Locate every blood parasite and identify its species.
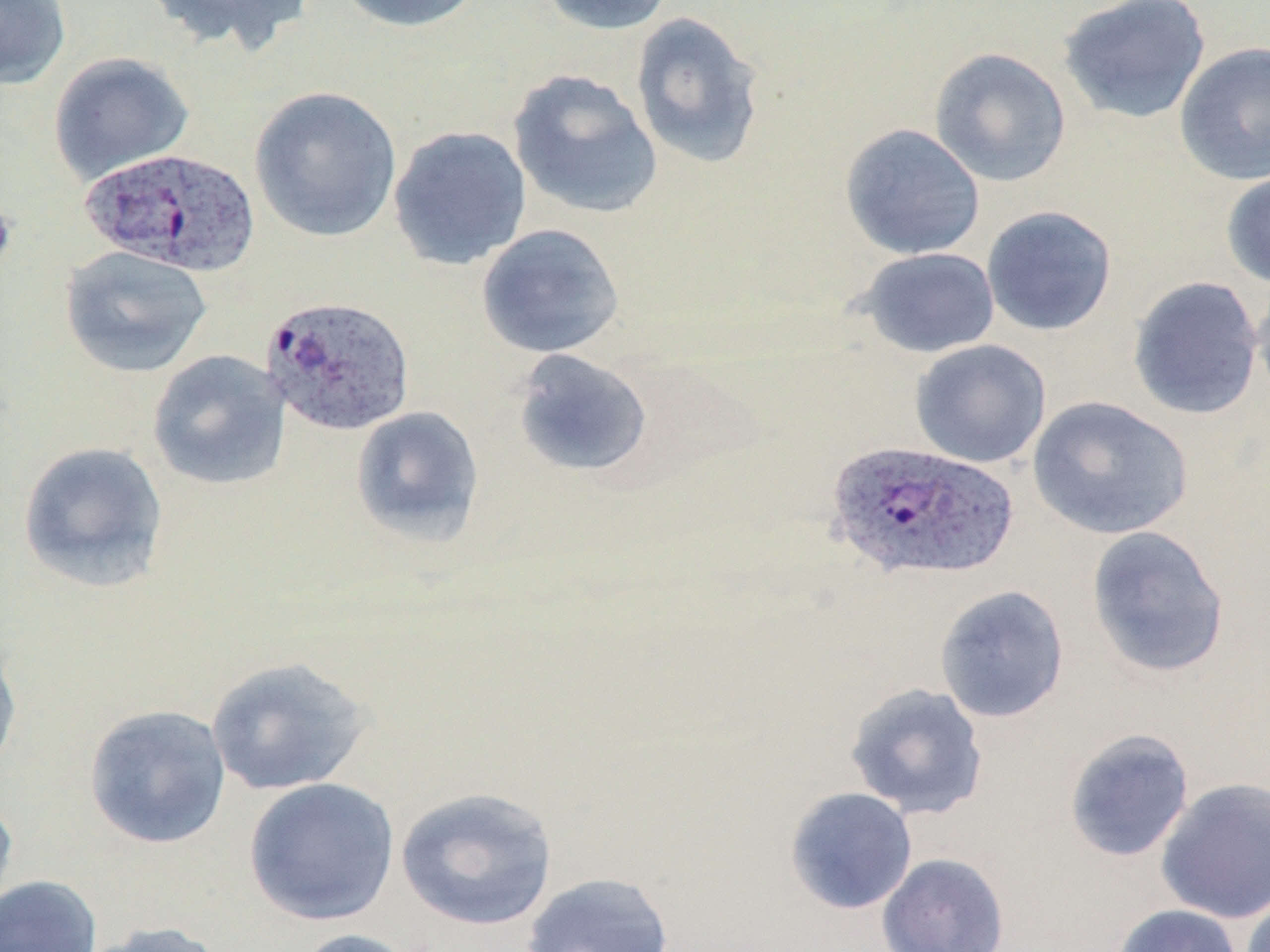
Approximate bounding boxes as named x1/y1/x2/y2 corners in pixels.
Plasmodium ovale-infected red blood cells: (x1=78, y1=148, x2=263, y2=277), (x1=260, y1=295, x2=416, y2=437), (x1=827, y1=440, x2=1018, y2=583).
No Plasmodium falciparum, Plasmodium malariae, Plasmodium vivax, Babesia divergens, or Trypanosoma brucei observed.

Summary:
  - Uninfected red blood cell locations: (x1=0, y1=0, x2=71, y2=89), (x1=143, y1=0, x2=314, y2=56), (x1=335, y1=0, x2=486, y2=33), (x1=534, y1=0, x2=677, y2=36), (x1=1057, y1=0, x2=1211, y2=124), (x1=629, y1=11, x2=767, y2=170), (x1=1174, y1=42, x2=1270, y2=185), (x1=928, y1=47, x2=1072, y2=188), (x1=48, y1=51, x2=194, y2=185), (x1=507, y1=69, x2=663, y2=220), (x1=249, y1=85, x2=402, y2=242), (x1=839, y1=123, x2=986, y2=260), (x1=387, y1=125, x2=532, y2=271), (x1=1220, y1=169, x2=1270, y2=289), (x1=981, y1=205, x2=1118, y2=336), (x1=476, y1=223, x2=625, y2=359), (x1=60, y1=245, x2=212, y2=379), (x1=856, y1=246, x2=1000, y2=358), (x1=1127, y1=276, x2=1265, y2=420), (x1=1252, y1=278, x2=1270, y2=413), (x1=909, y1=339, x2=1051, y2=469), (x1=511, y1=348, x2=654, y2=479), (x1=147, y1=349, x2=291, y2=491), (x1=1027, y1=395, x2=1194, y2=540), (x1=350, y1=405, x2=485, y2=547), (x1=16, y1=441, x2=170, y2=593), (x1=1085, y1=525, x2=1230, y2=679), (x1=934, y1=584, x2=1070, y2=724), (x1=0, y1=635, x2=23, y2=781), (x1=204, y1=655, x2=374, y2=797), (x1=844, y1=682, x2=989, y2=820), (x1=83, y1=704, x2=231, y2=849), (x1=1063, y1=727, x2=1195, y2=863), (x1=243, y1=777, x2=400, y2=926), (x1=1155, y1=778, x2=1270, y2=923), (x1=395, y1=786, x2=559, y2=931), (x1=784, y1=787, x2=918, y2=915), (x1=0, y1=791, x2=19, y2=924), (x1=876, y1=852, x2=1010, y2=952), (x1=521, y1=871, x2=675, y2=952), (x1=0, y1=874, x2=102, y2=952), (x1=1239, y1=889, x2=1270, y2=952), (x1=1111, y1=903, x2=1244, y2=952), (x1=79, y1=920, x2=230, y2=952), (x1=290, y1=928, x2=425, y2=952)
  - Slide-level diagnosis: Plasmodium ovale
  - Field of view: one of a larger specimen
  - Magnification: 1000x
  - Image size: 1270×952 pixels
  - Modality: optical microscopy
  - Preparation: thin blood smear
  - Stain: May-Grünwald-Giemsa